Comment on the morphology of the red blood cells.
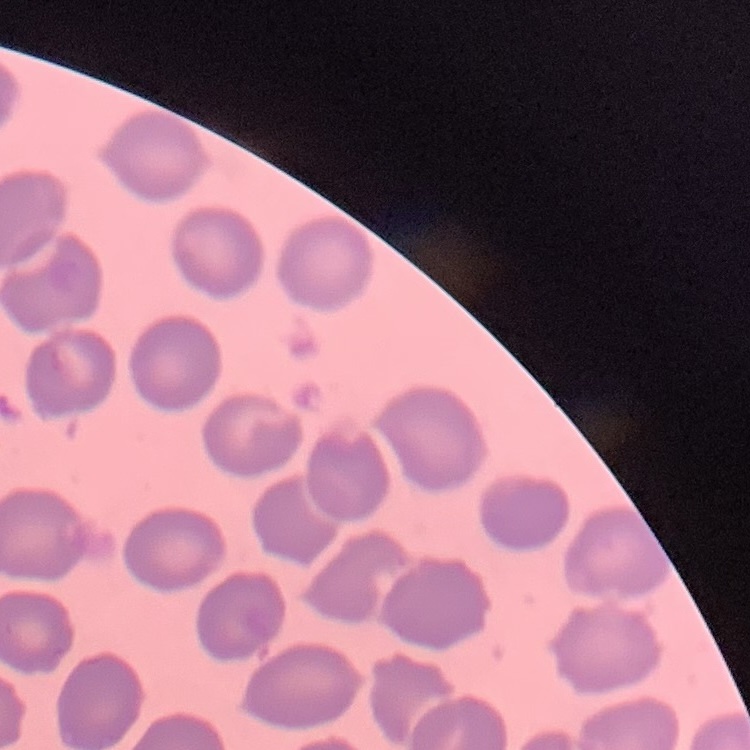

They show no rouleaux formation.

Summary:
  - Stain: Field's or Giemsa
  - Image type: square crop of a larger photomicrograph
  - Preparation: thin blood film